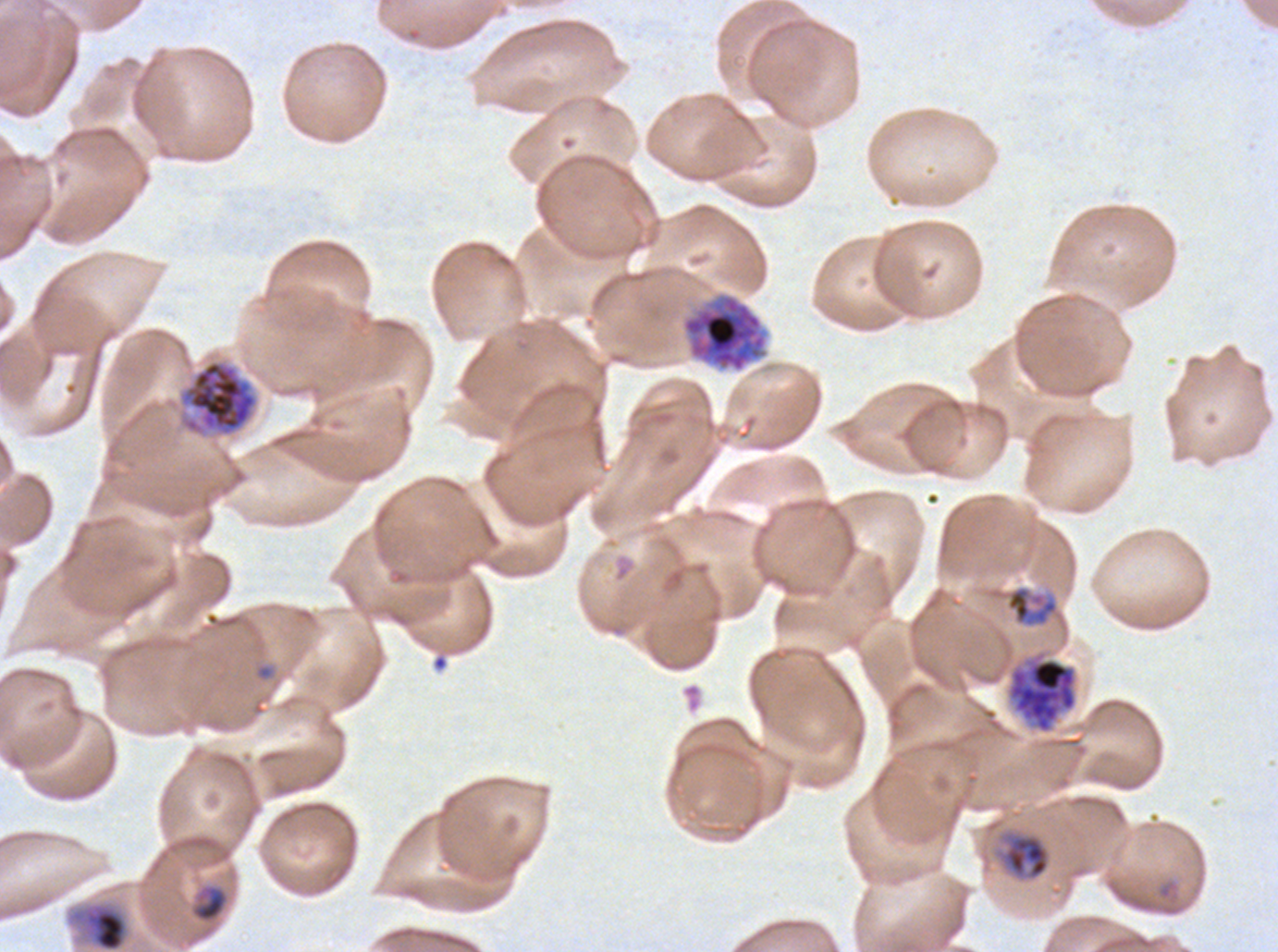

Approximate bounding boxes as [x1, y1, x2, y2] in pixels. Mid trophozoite locations: [1005, 585, 1059, 628], [997, 830, 1051, 882], [65, 900, 132, 951]. Ring locations: [253, 663, 276, 682]. Early schizont locations: [681, 293, 768, 372], [177, 358, 260, 439], [1008, 657, 1077, 733]. Late-ring/early-trophozoite locations: [190, 884, 229, 923]. One sub-image of a larger composite. Image is 1278×952 pixels. Ex-vivo P. falciparum culture from a patient in The Gambia, grown for 24 to 48 hours. Giemsa-stained preparation. Thin blood smear. Life-cycle stages observed: ring, late-ring/early-trophozoite, mid trophozoite, early schizont.